Outline each Plasmodium ovale-infected red blood cell.
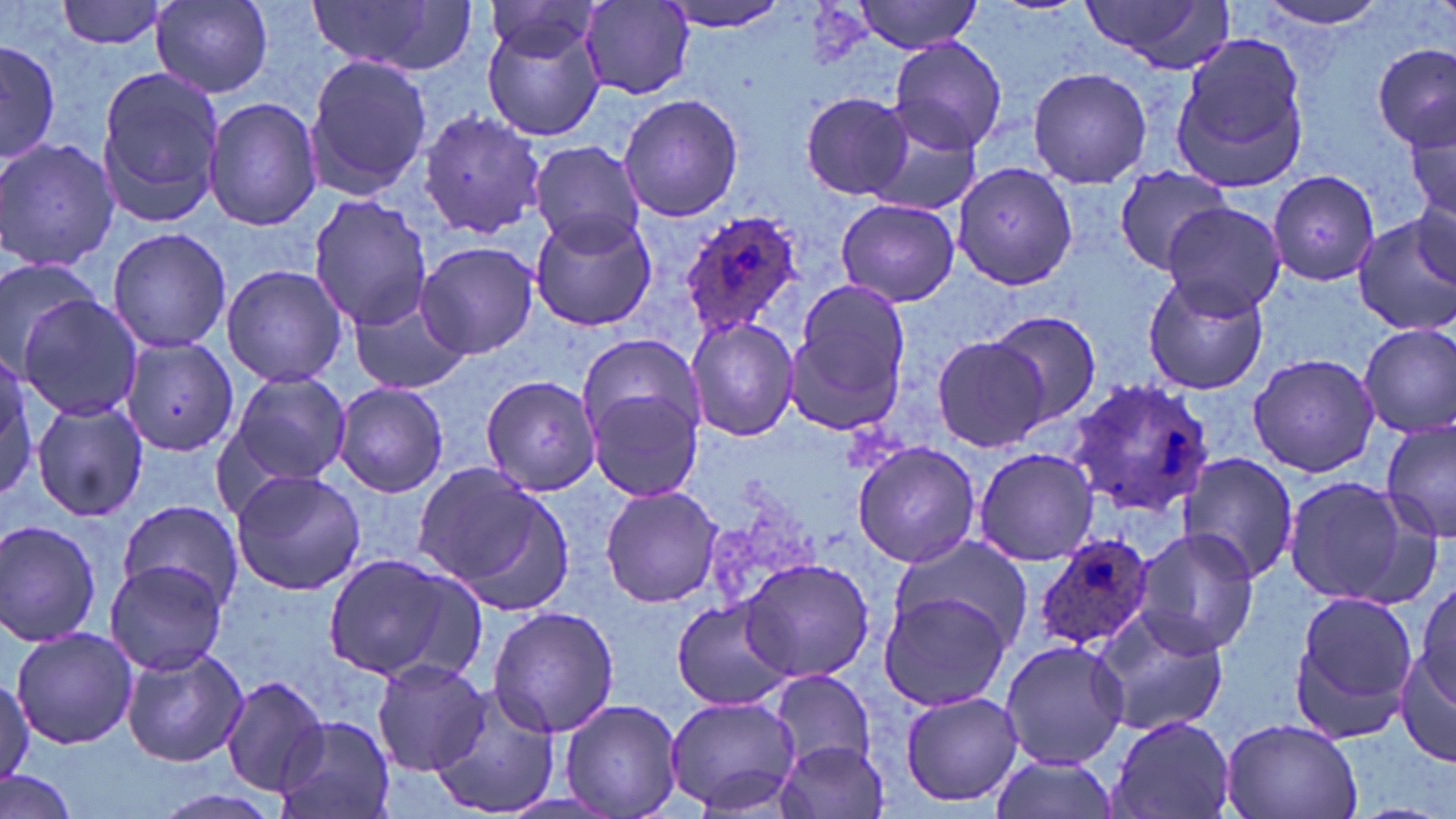
Approximate bounding boxes as (x1,y1)-(x2,y2) corner pairs in pixels.
Plasmodium ovale-infected red blood cells: (681,209)-(806,339), (1066,377)-(1217,516), (1031,533)-(1157,653).

Uninfected red blood cell locations: (56,0)-(175,50), (152,0)-(274,97), (305,0)-(477,75), (658,0)-(794,33), (848,0)-(988,52), (1254,0)-(1392,35), (1079,1)-(1235,69), (484,2)-(599,69), (579,2)-(696,99), (483,17)-(605,142), (1171,33)-(1314,191), (887,35)-(1007,154), (1,37)-(59,166), (1374,42)-(1455,151), (304,53)-(432,200), (1026,66)-(1154,191), (95,67)-(226,228), (799,92)-(915,200), (618,93)-(742,223), (204,97)-(323,230), (417,109)-(548,238), (1404,111)-(1456,232), (864,118)-(983,216), (0,136)-(119,275), (528,140)-(649,253), (952,162)-(1077,288), (1112,164)-(1235,275), (1268,170)-(1381,288), (307,194)-(434,332), (834,197)-(960,307), (1410,197)-(1456,288), (1161,202)-(1285,317), (528,209)-(655,331), (1350,214)-(1456,336), (106,225)-(232,355), (416,241)-(539,360), (0,257)-(108,369), (220,263)-(347,388), (1141,268)-(1271,397), (785,279)-(912,435), (347,292)-(471,395), (16,294)-(143,423), (986,311)-(1101,424), (687,316)-(800,442), (1357,323)-(1456,439), (576,331)-(706,456), (119,336)-(240,456), (933,337)-(1051,453), (0,349)-(43,500), (1247,352)-(1382,479), (225,369)-(351,489), (481,375)-(600,495), (332,382)-(448,497), (589,391)-(705,502), (31,399)-(148,522), (1381,416)-(1456,542), (852,442)-(982,569), (972,447)-(1100,567), (1179,452)-(1301,583), (412,465)-(567,607), (230,470)-(366,595), (1283,475)-(1430,609), (600,485)-(724,608), (118,499)-(247,610), (0,518)-(104,647), (1131,527)-(1263,657), (886,533)-(1030,655), (318,552)-(468,684), (104,558)-(229,678), (738,558)-(877,683), (1413,574)-(1455,717), (1288,590)-(1418,738), (878,593)-(1012,714), (670,599)-(796,712), (1089,605)-(1231,737), (488,606)-(620,738), (1249,621)-(1400,777), (11,627)-(138,749), (998,639)-(1130,769), (1395,643)-(1456,770), (120,647)-(247,767), (372,658)-(487,774), (767,669)-(876,772), (221,675)-(331,795), (0,676)-(34,784), (429,687)-(563,815), (898,690)-(1024,806), (662,695)-(804,815), (560,698)-(683,819), (273,716)-(395,819), (1107,716)-(1237,819), (1220,717)-(1364,819), (776,738)-(891,819), (986,754)-(1119,819), (0,768)-(80,819), (145,789)-(284,819). Slide-level diagnosis: Plasmodium ovale. May-Grünwald-Giemsa-stained preparation. 1000x magnification. Image is 1456×819 pixels. Optical microscopy. Thin blood film. Single field of view.